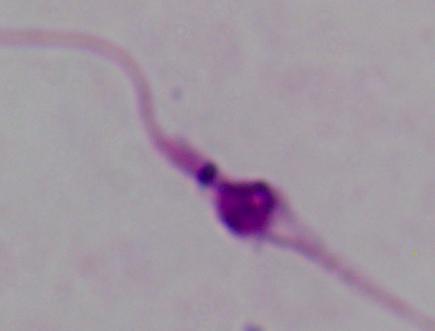
Summary:
  - Magnification: 1000x
  - Identification: Leishmania
  - Modality: micrograph